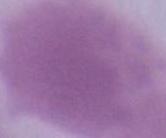

modality = photomicrograph
identification = red blood cell
magnification = 1000x